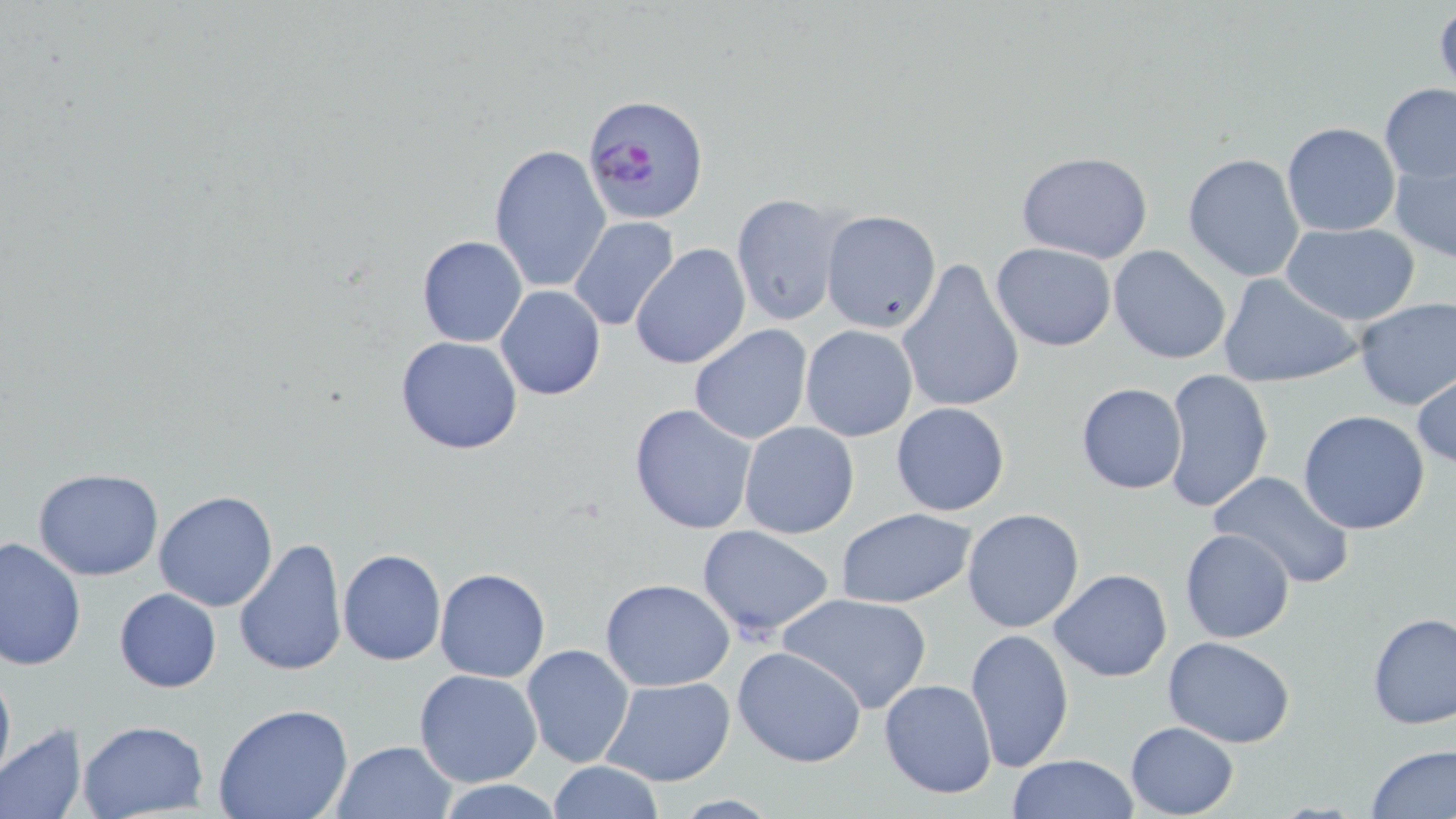

Approximate bounding boxes as (x1, y1, x2, y2) in pixels. Plasmodium falciparum-infected red blood cell locations: (585, 95, 710, 227). Uninfected red blood cell locations: (1379, 83, 1456, 184), (1281, 121, 1401, 237), (490, 144, 610, 295), (1015, 150, 1155, 261), (1389, 150, 1456, 268), (1182, 152, 1306, 282), (730, 194, 847, 327), (821, 209, 942, 334), (568, 217, 680, 332), (1280, 223, 1423, 326), (415, 236, 528, 348), (629, 242, 751, 371), (990, 242, 1117, 351), (1107, 245, 1233, 365), (897, 258, 1025, 415), (1217, 273, 1365, 389), (496, 285, 606, 400), (1353, 298, 1456, 410), (688, 325, 813, 445), (800, 325, 919, 442), (394, 335, 524, 455), (1412, 368, 1456, 472), (1162, 369, 1274, 513), (1075, 381, 1187, 495), (890, 402, 1011, 518), (629, 403, 758, 535), (1298, 410, 1431, 535), (739, 420, 859, 538), (33, 468, 164, 580), (1208, 469, 1357, 587), (152, 491, 278, 612), (835, 508, 975, 607), (961, 508, 1085, 633), (696, 524, 836, 638), (1178, 529, 1295, 644), (0, 535, 85, 672), (232, 537, 348, 678), (338, 548, 447, 665), (433, 568, 550, 682), (1047, 569, 1173, 682), (600, 577, 735, 691), (113, 588, 222, 693), (777, 594, 932, 715), (1365, 612, 1455, 731), (966, 628, 1072, 771), (1162, 637, 1296, 748), (520, 645, 635, 768), (732, 645, 869, 768), (0, 660, 14, 787), (414, 670, 543, 787), (599, 677, 736, 787), (878, 678, 997, 799), (212, 704, 354, 819), (77, 720, 208, 819), (1125, 721, 1240, 817), (0, 725, 88, 819), (332, 739, 457, 819), (1366, 745, 1456, 818), (1007, 754, 1140, 818), (544, 761, 665, 818), (434, 780, 568, 818). Slide-level diagnosis: Plasmodium falciparum. Single field of view. May-Grünwald-Giemsa-stained preparation. Light microscopy. 1000x magnification. Image is 1456×819 pixels. Thin blood smear.